Locate every Plasmodium parasite.
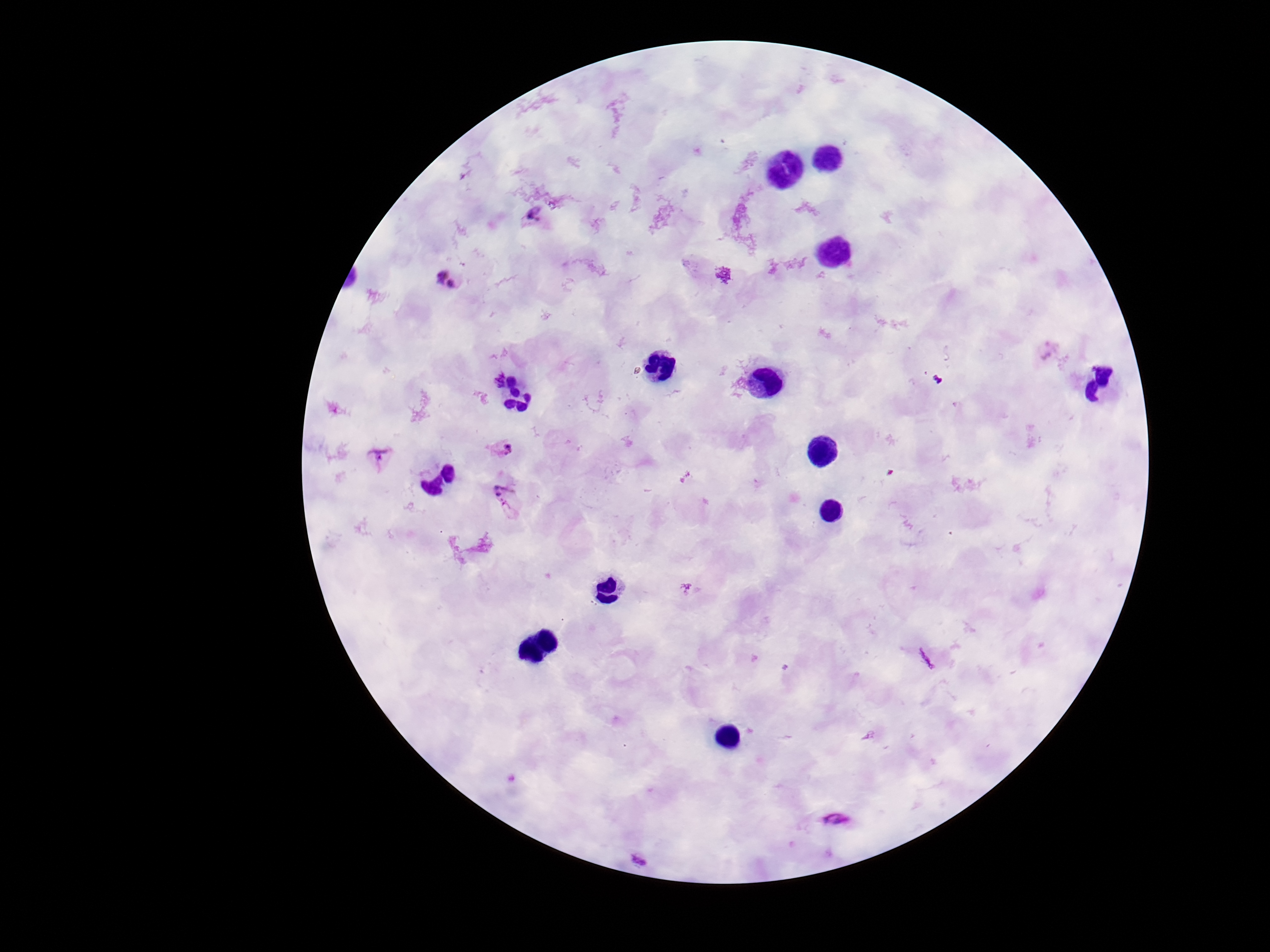
Approximate object centers, in pixels from the top-left corner.
Plasmodium parasites: (x=533, y=217), (x=448, y=281), (x=499, y=448), (x=379, y=456), (x=507, y=502), (x=839, y=822), (x=639, y=860).

Smartphone photograph taken through the microscope eyepiece. Thick peripheral-blood smear. Single field of view. 100x magnification. Image is 1270×952 pixels. Patient malaria status: infected. Giemsa-stained preparation.